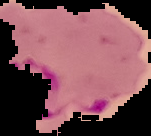

From a thin blood film. Malaria status: parasitized. Cell region segmented out of the field of view; the surrounding area is masked to black. Image is 151×136 pixels.